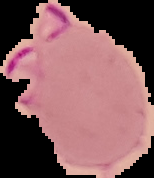
Result: Plasmodium parasites detected. From a thin blood smear. The area outside the segmented cell region is set to black. Image is 154×178 pixels.